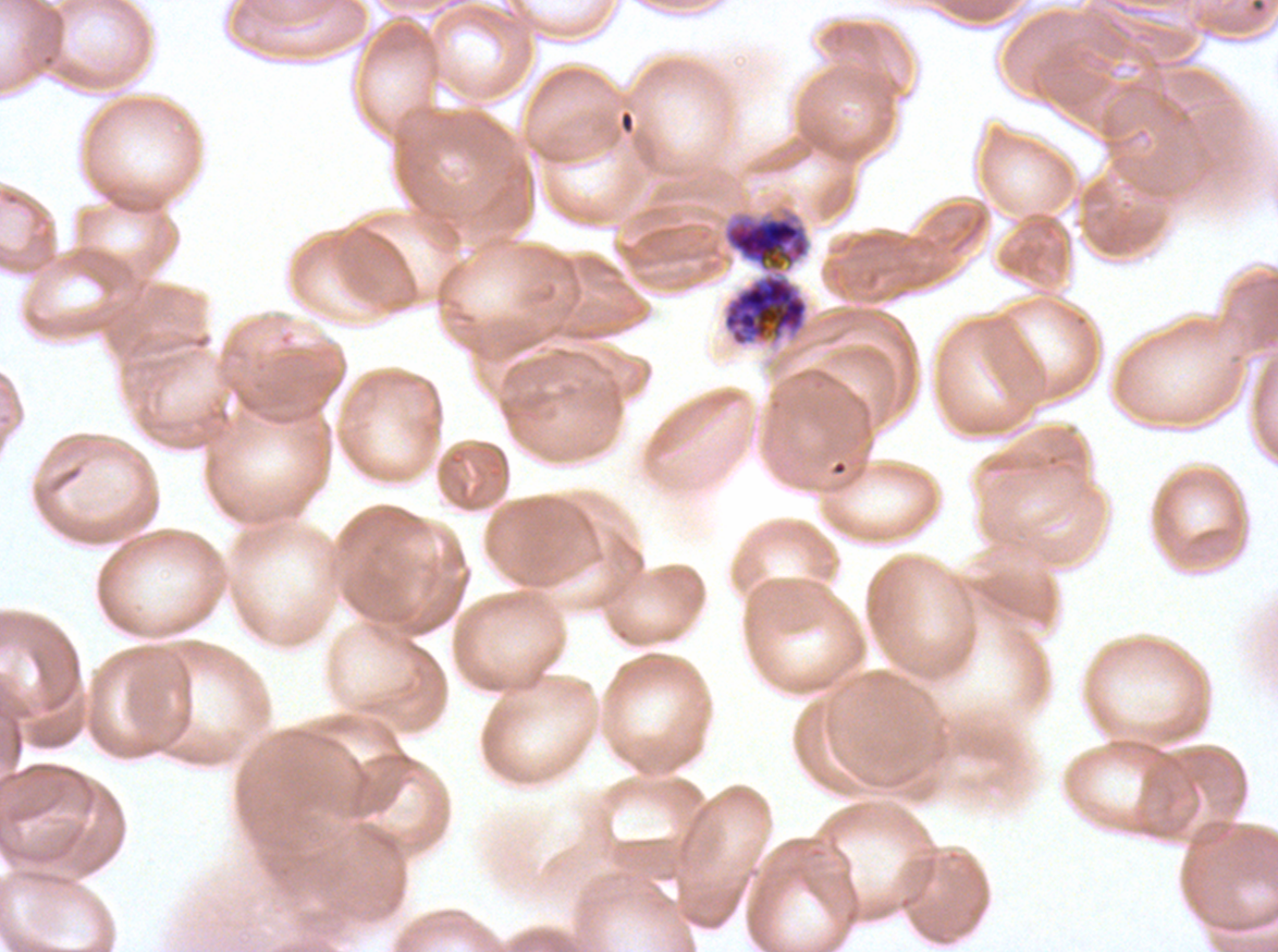

field_of_view: one sub-image of a larger composite
life_cycle_stages_observed: early schizont, segmenter
preparation: thin blood film
specimen: Plasmodium falciparum cultured ex vivo for 24 to 48 hours, from a patient in The Gambia
early_schizont_locations: 'approximate bounding boxes as [x1, y1, x2, y2] in pixels: [722, 215, 810, 347]'
image_size: 1278×952 pixels
segmenter_locations: 'approximate bounding boxes as [x1, y1, x2, y2] in pixels: [722, 215, 810, 347] (two touching objects share this one region)'
stain: Giemsa